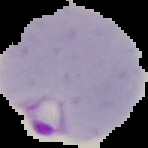

Result: malaria parasites identified. Segmented cell region on a black background. Image is 148×148 pixels. From a thin blood smear.